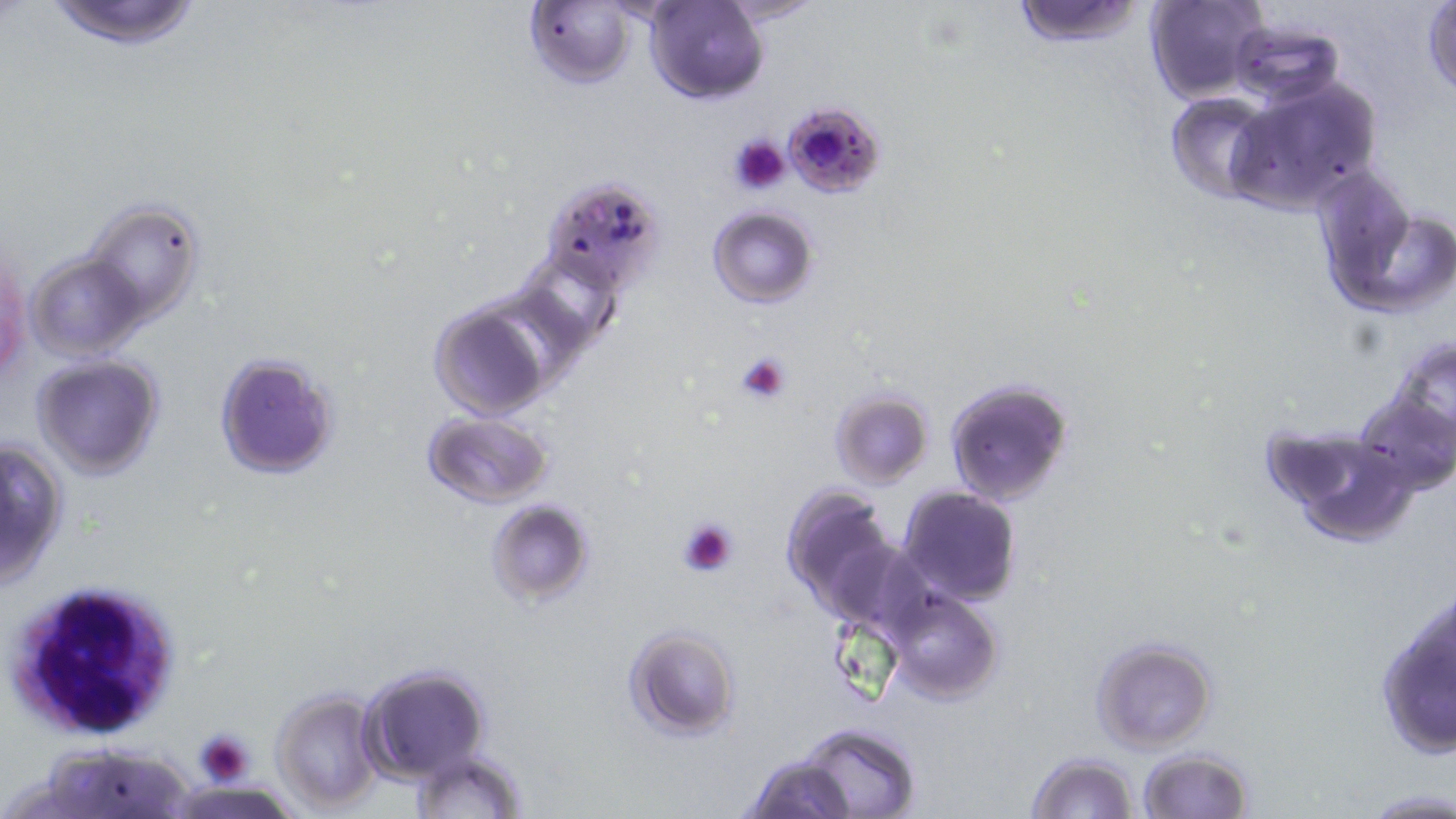

Summary:
  - Coordinate format: approximate bounding boxes as (x1, y1, x2, y2) in pixels
  - Plasmodium falciparum-infected red blood cell locations: (781, 102, 888, 198)
  - White blood cell locations: (5, 579, 187, 742)
  - Platelet locations: (728, 132, 791, 196), (735, 351, 793, 406), (677, 517, 740, 579), (193, 730, 255, 785)
  - Uninfected red blood cell locations: (43, 0, 206, 50), (646, 0, 766, 102), (716, 0, 829, 25), (1011, 0, 1145, 48), (1148, 0, 1271, 104), (1423, 1, 1455, 102), (525, 2, 636, 88), (1231, 19, 1343, 109), (1227, 79, 1382, 212), (1167, 93, 1277, 203), (1313, 173, 1454, 320), (540, 175, 666, 293), (81, 201, 204, 326), (708, 207, 818, 307), (0, 238, 28, 386), (25, 251, 150, 362), (427, 301, 549, 419), (1385, 333, 1456, 455), (214, 352, 339, 479), (32, 353, 165, 479), (945, 378, 1075, 506), (1355, 387, 1454, 497), (829, 389, 933, 487), (422, 411, 553, 509), (1272, 428, 1420, 544), (1, 436, 69, 586), (779, 484, 903, 624), (897, 487, 1021, 606), (486, 500, 594, 605), (883, 589, 1004, 705), (1372, 593, 1454, 762), (623, 625, 741, 739), (1089, 636, 1219, 753), (360, 663, 492, 781), (271, 686, 384, 813), (797, 724, 922, 818), (179, 729, 276, 796), (40, 743, 195, 819), (405, 748, 524, 817), (1137, 748, 1254, 819), (1026, 751, 1142, 819), (741, 752, 858, 819), (1360, 789, 1454, 818)
  - Slide-level diagnosis: Plasmodium falciparum
  - Modality: optical microscopy
  - Magnification: 1000x
  - Image size: 1456×819 pixels
  - Stain: May-Grünwald-Giemsa
  - Field of view: single
  - Preparation: thin blood smear